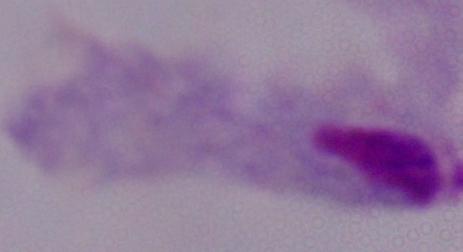

identification = trichomonad
magnification = 1000x
modality = micrograph